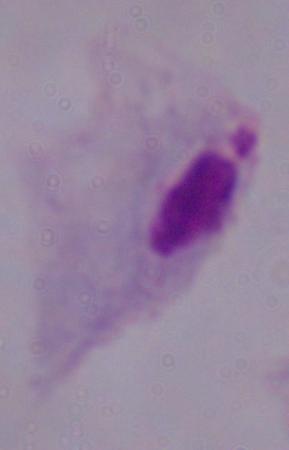
identification: trichomonad
modality: micrograph
magnification: 1000x